Describe the morphology of the red blood cells.
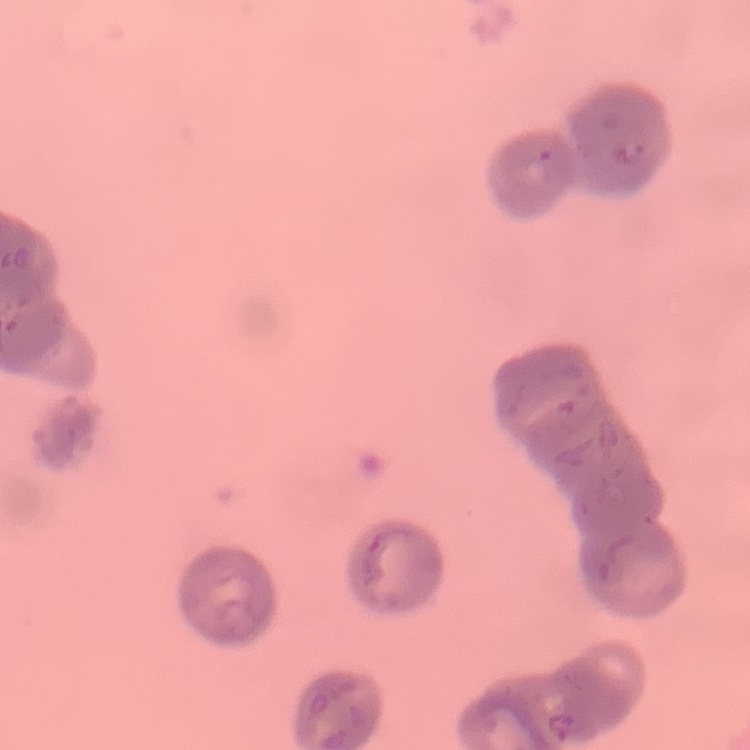
Rouleaux formation.

Thin peripheral smear. One tile cut from a larger photomicrograph. Stained with either Field's or Giemsa.